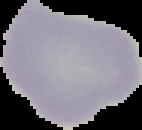
Result: negative for malaria parasites. Segmented cell region on a black background. From a thin blood smear. Image is 142×130 pixels.